State the blood parasite species.
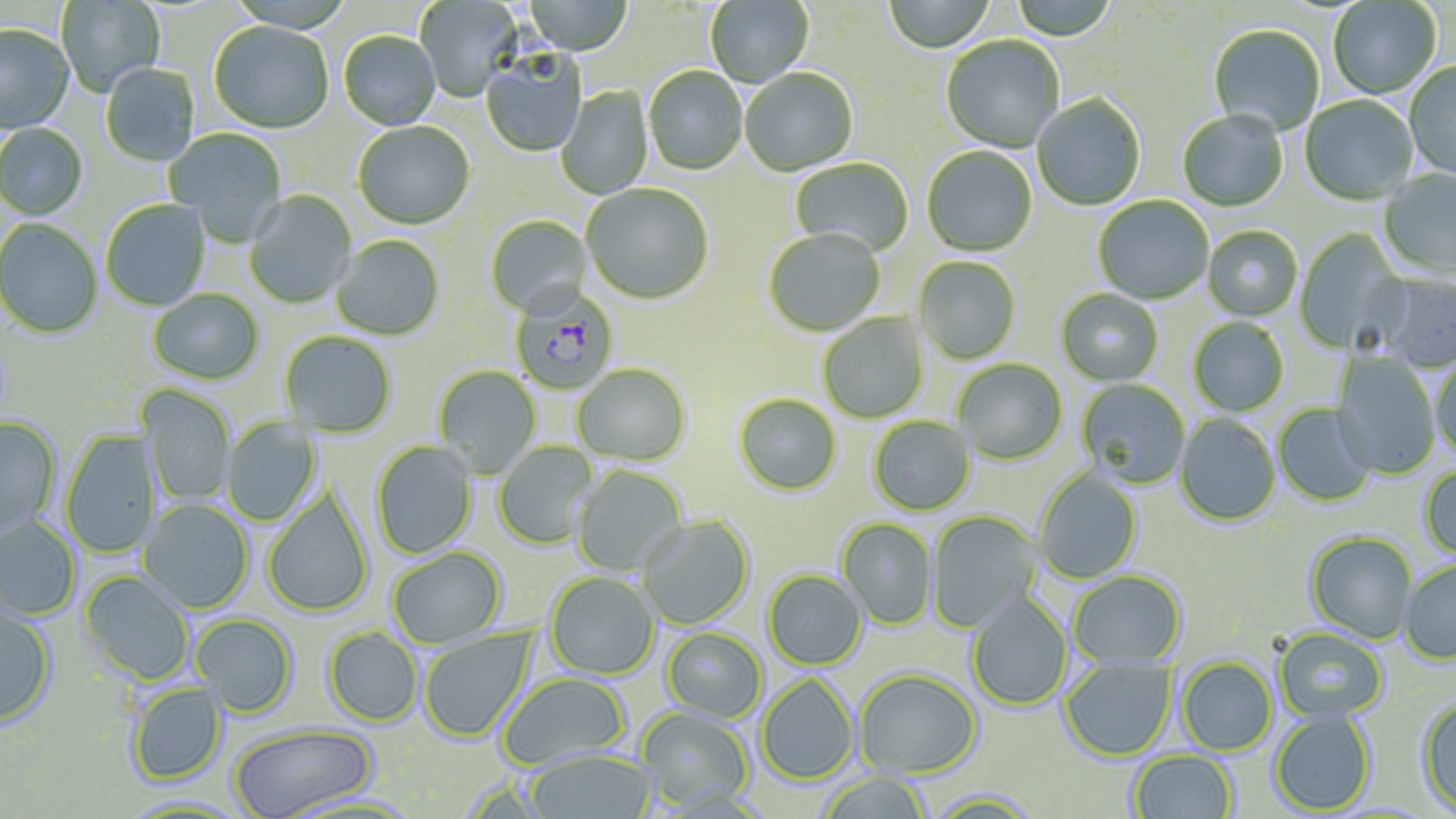
Plasmodium falciparum.

Approximate bounding boxes as (x1, y1, x2, y2) in pixels. Plasmodium falciparum-infected red blood cell locations: (509, 289, 619, 396). Uninfected red blood cell locations: (524, 0, 632, 57), (705, 0, 814, 88), (884, 0, 996, 54), (1008, 0, 1119, 42), (1328, 0, 1441, 100), (56, 1, 166, 98), (415, 1, 523, 102), (208, 22, 333, 135), (0, 25, 74, 134), (1208, 25, 1326, 137), (338, 32, 441, 131), (941, 36, 1065, 154), (480, 51, 588, 158), (1404, 62, 1456, 182), (100, 64, 200, 168), (643, 68, 748, 176), (739, 69, 859, 178), (555, 86, 654, 200), (1032, 95, 1146, 212), (1300, 96, 1418, 207), (1177, 112, 1289, 213), (353, 122, 475, 231), (0, 124, 88, 221), (165, 128, 287, 245), (922, 147, 1037, 258), (790, 159, 913, 256), (1378, 170, 1456, 281), (581, 185, 714, 306), (244, 190, 357, 309), (1093, 196, 1213, 305), (101, 200, 211, 311), (485, 216, 592, 319), (0, 219, 103, 339), (1202, 226, 1303, 322), (1294, 228, 1408, 356), (764, 229, 886, 338), (331, 236, 445, 342), (913, 257, 1021, 364), (1374, 274, 1456, 374), (147, 289, 264, 385), (1056, 289, 1164, 388), (817, 313, 929, 423), (1188, 317, 1289, 417), (279, 331, 397, 438), (1330, 352, 1441, 479), (1429, 356, 1456, 464), (953, 359, 1067, 466), (571, 364, 691, 468), (432, 366, 542, 478), (1076, 379, 1190, 490), (138, 385, 236, 505), (733, 394, 841, 497), (1272, 404, 1376, 507), (1174, 414, 1281, 528), (868, 416, 975, 516), (0, 417, 61, 539), (222, 418, 322, 526), (60, 430, 161, 558), (370, 441, 478, 560), (494, 441, 600, 550), (571, 465, 689, 576), (1419, 466, 1456, 561), (1033, 468, 1143, 585), (262, 489, 374, 617), (138, 499, 254, 614), (926, 511, 1041, 633), (636, 514, 755, 630), (0, 515, 82, 621), (836, 518, 938, 630), (1305, 532, 1417, 644), (387, 547, 507, 650), (1399, 559, 1456, 665), (762, 570, 867, 670), (79, 571, 195, 685), (1068, 571, 1186, 670), (544, 572, 660, 681), (967, 592, 1072, 711), (0, 601, 57, 727), (190, 613, 299, 718), (322, 627, 423, 726), (417, 627, 537, 743), (661, 628, 767, 724), (1273, 628, 1388, 723), (1059, 655, 1177, 761), (1177, 657, 1277, 756), (853, 668, 982, 779), (497, 672, 631, 772), (756, 674, 858, 785), (126, 682, 227, 785), (1416, 696, 1456, 816), (635, 706, 756, 812), (1270, 711, 1376, 815), (229, 723, 377, 819), (525, 749, 657, 818), (1127, 750, 1238, 818), (817, 772, 932, 819), (924, 789, 1045, 817). Captured at 1000x magnification. Light microscopy. Thin blood smear. One field of a larger specimen. Image is 1456×819 pixels. May-Grünwald-Giemsa-stained preparation.